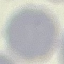

{
  "malaria_status": "uninfected",
  "image_type": "automatically extracted cell patch, resized to 64 × 64 pixels",
  "stain": "Giemsa",
  "preparation": "thin blood smear",
  "capture": "smartphone through the microscope eyepiece"
}